Outline each Plasmodium malariae-infected red blood cell.
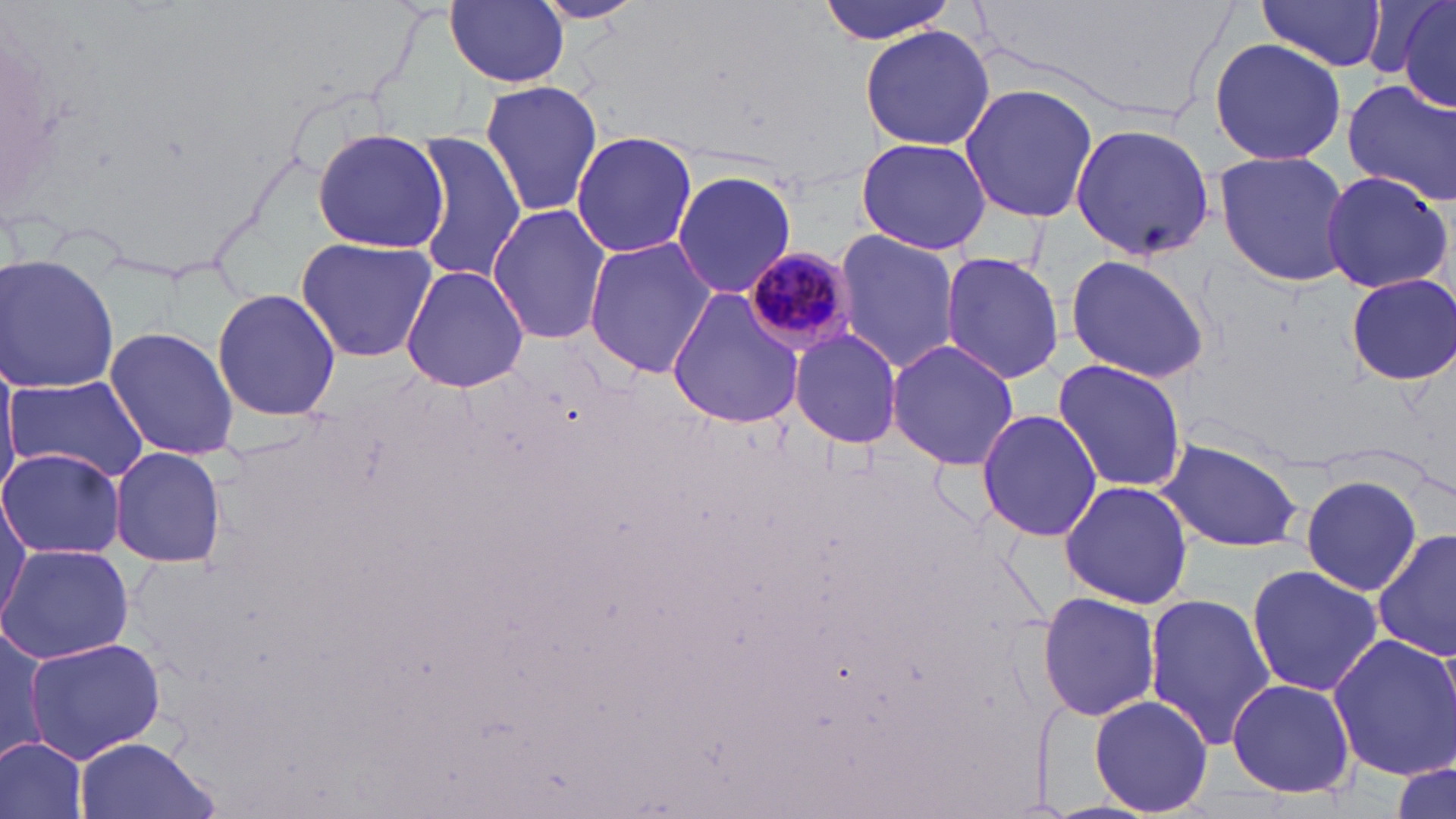
Approximate bounding boxes as [x1, y1, x2, y2] in pixels.
Plasmodium malariae-infected red blood cells: [739, 249, 855, 359].

Summary:
  - Uninfected red blood cell locations: [443, 0, 571, 87], [528, 0, 649, 25], [818, 0, 959, 44], [1254, 0, 1390, 72], [1390, 2, 1456, 110], [858, 24, 996, 151], [1208, 38, 1348, 168], [1343, 78, 1455, 206], [478, 81, 604, 219], [957, 85, 1101, 222], [1068, 122, 1215, 259], [309, 129, 447, 252], [571, 130, 698, 258], [409, 133, 524, 287], [853, 135, 993, 256], [1214, 151, 1355, 287], [670, 169, 799, 301], [1318, 170, 1453, 296], [488, 205, 613, 346], [833, 229, 961, 374], [582, 236, 716, 379], [293, 238, 439, 362], [941, 251, 1066, 386], [0, 252, 121, 394], [1064, 253, 1211, 383], [400, 264, 528, 393], [1345, 273, 1455, 384], [667, 286, 810, 429], [212, 287, 341, 423], [106, 325, 237, 461], [790, 330, 903, 449], [886, 339, 1021, 469], [1052, 357, 1187, 494], [0, 362, 23, 493], [7, 374, 149, 487], [975, 407, 1102, 542], [1153, 434, 1306, 553], [110, 447, 229, 570], [0, 449, 126, 561], [1297, 473, 1425, 596], [1060, 479, 1194, 609], [0, 494, 31, 615], [1374, 528, 1456, 663], [0, 542, 134, 664], [1245, 565, 1386, 697], [1038, 591, 1163, 722], [1141, 592, 1278, 751], [1, 625, 51, 768], [1327, 633, 1456, 783], [26, 636, 165, 762], [1227, 677, 1356, 799], [1087, 694, 1214, 816], [70, 735, 220, 819], [0, 736, 88, 819], [1387, 759, 1455, 818]
  - Slide-level diagnosis: Plasmodium malariae
  - Magnification: 1000x
  - Stain: May-Grünwald-Giemsa
  - Image size: 1456×819 pixels
  - Preparation: thin blood smear
  - Modality: optical microscopy
  - Field of view: one of a larger specimen